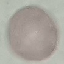

Summary:
  - Result: no malaria parasites seen
  - Stain: Giemsa
  - Preparation: thin blood smear
  - Image type: automatically extracted cell patch, resized to 64 × 64 pixels
  - Capture: smartphone camera at the microscope eyepiece